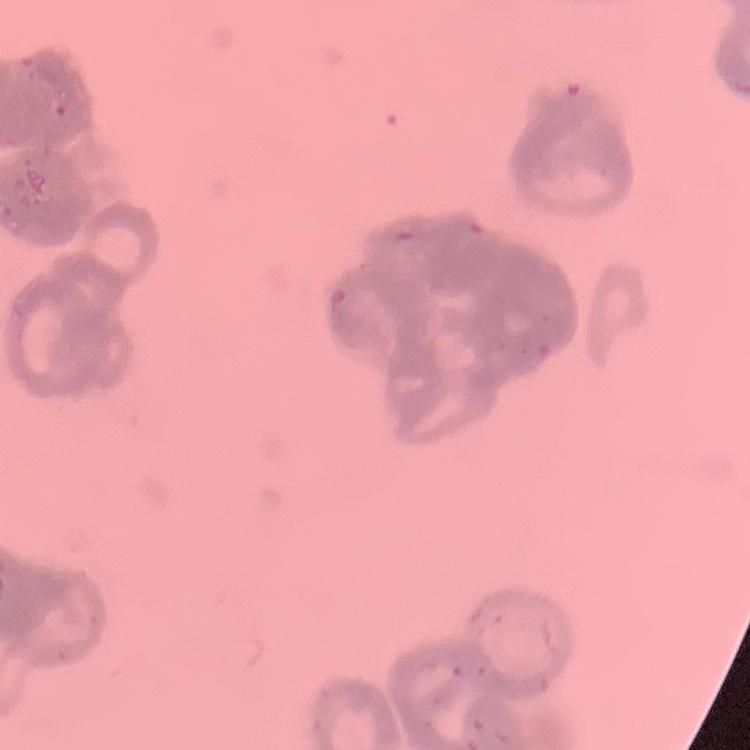

red blood cell morphology = rouleaux formation
image type = square crop of a larger photomicrograph
preparation = thin blood smear
stain = Field's or Giemsa